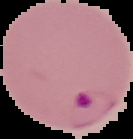
malaria status = parasitized
image type = segmented cell region on a black background
preparation = thin blood film
image size = 133×139 pixels